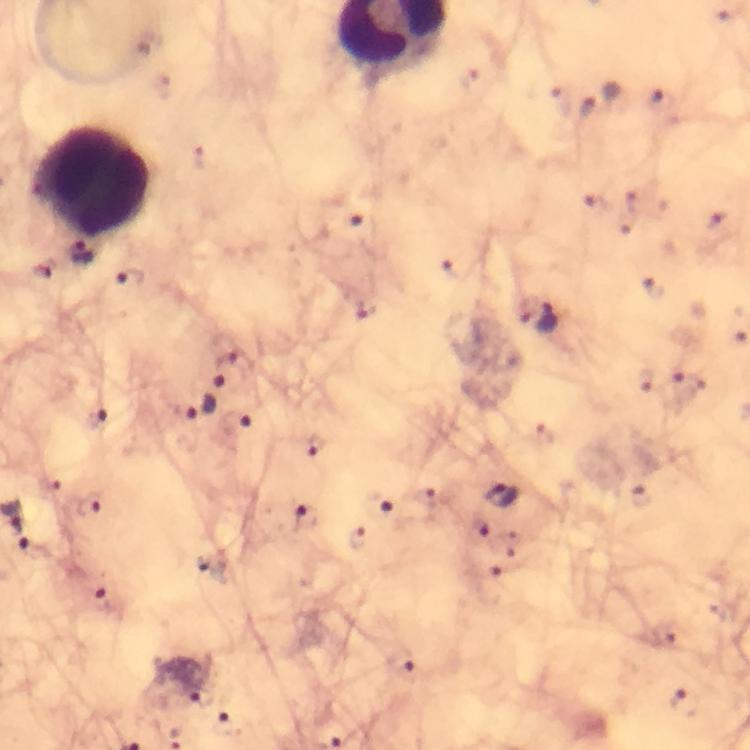
Approximate centers as [x, y] in pixels. Malaria parasite locations: [668, 101], [587, 110], [365, 229], [81, 253], [129, 281], [362, 306], [549, 320], [642, 380], [686, 383], [217, 393], [96, 419], [502, 494], [375, 505], [305, 520], [101, 600], [198, 694], [684, 701], [227, 726]. Leukocyte locations: [93, 182]. From a diagnostic examination for malaria. Image is 750×750 pixels. Cropped region of a single field of view. Thick blood smear. Giemsa-stained preparation. Smartphone photograph taken through a microscope. Immersion oil applied. At 100x magnification.